Identify the parasite.
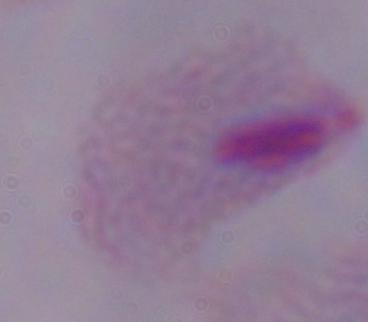

This is a trichomonad.

Summary:
  - Modality: micrograph
  - Magnification: 1000x